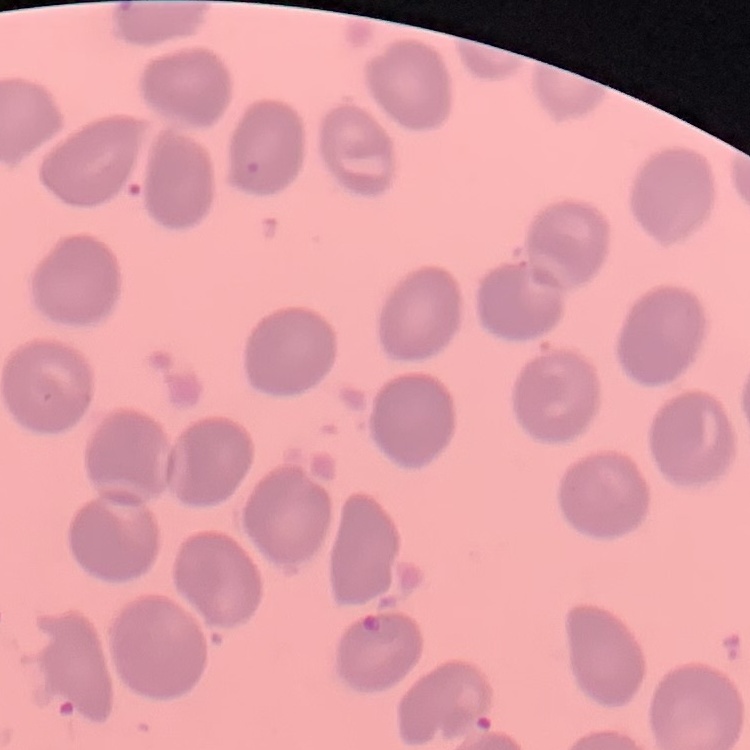

The erythrocytes show no rouleaux formation. One tile cut from a larger photomicrograph. Field's or Giemsa stain. Thin blood smear.